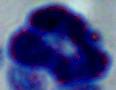

Summary:
  - Identification: white blood cell
  - Magnification: 1000x
  - Modality: photomicrograph